Report the malaria status of this cell.
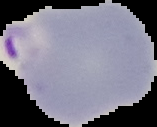

It is parasitized.

image size = 157×127 pixels
image type = segmented cell region with the area outside set to black
preparation = thin blood smear